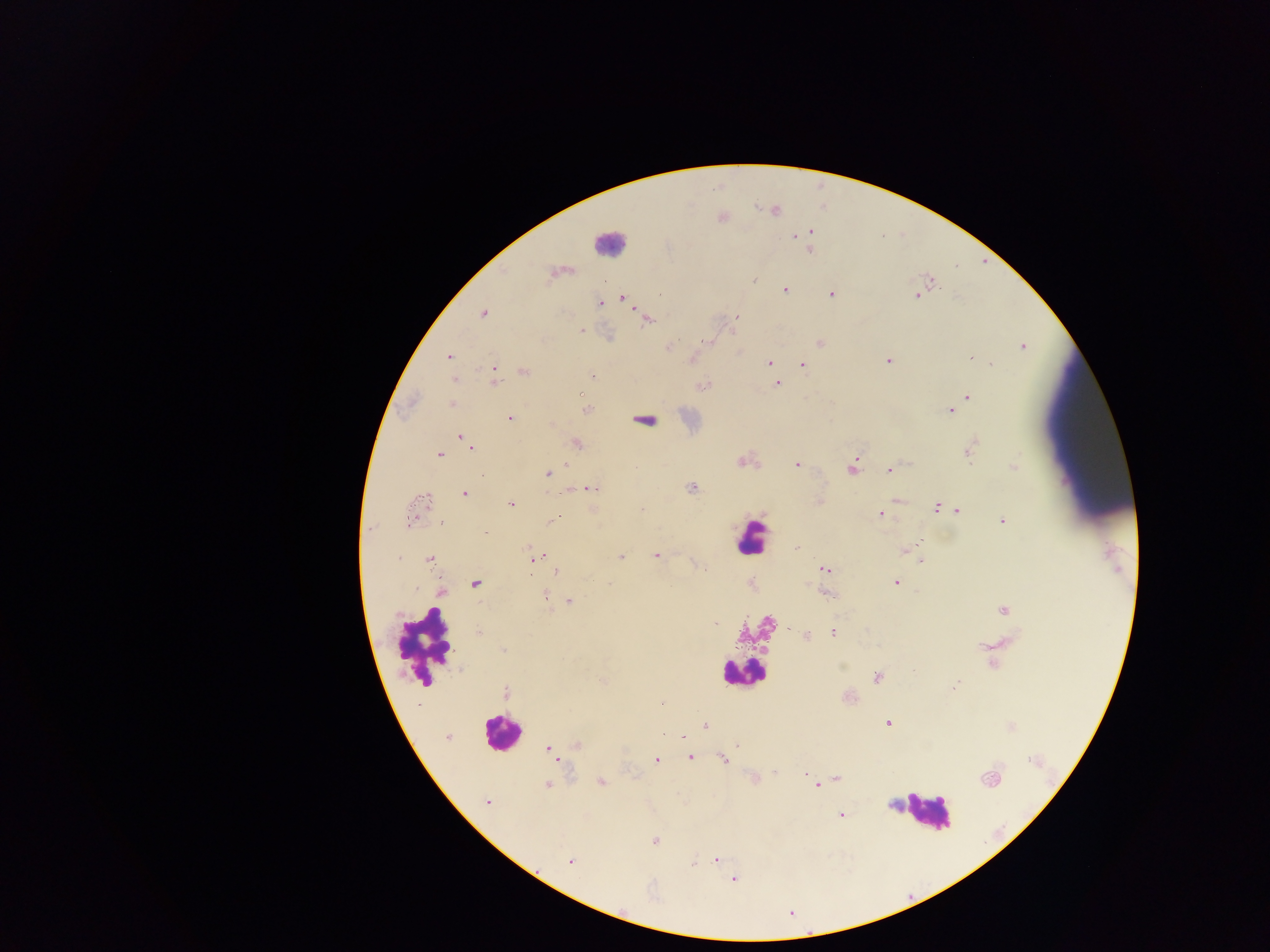

Plasmodium parasite locations = approximate centers as x y in pixels: 722 217; 811 231; 793 237; 669 248; 808 250; 563 273; 552 275; 755 280; 931 282; 786 291; 919 294; 831 295; 622 296; 914 296; 618 299; 627 300; 599 303; 483 313; 564 313; 648 321; 582 328; 819 343; 670 346; 1023 346; 971 357; 449 359; 886 359; 768 360; 803 363; 992 364; 495 373; 593 373; 589 378; 777 384; 581 395; 968 398; 451 405; 587 408; 949 410; 643 418; 512 419; 462 436; 577 443; 973 443; 469 447; 968 452; 439 454; 741 461; 798 464; 567 465; 1012 465; 851 467; 888 470; 546 472; 592 488; 691 488; 464 493; 420 503; 511 503; 642 509; 935 509; 958 511; 881 514; 553 519; 1003 520; 485 533; 915 541; 524 546; 902 551; 542 555; 656 556; 621 557; 534 559; 919 559; 431 561; 701 567; 823 569; 556 572; 896 582; 476 583; 608 583; 752 583; 807 586; 440 592; 829 594; 546 597; 569 599; 1001 609; 717 623; 833 631; 806 636; 980 646; 503 648; 990 664; 841 665; 877 678; 601 679; 956 684; 661 702; 414 704; 416 704; 887 723; 706 724; 1010 726; 684 736; 447 738; 574 745; 735 745; 547 748; 689 757; 655 759; 721 759; 774 771; 803 771; 753 777; 807 777; 989 778; 837 780; 832 781; 600 782; 548 785; 818 786; 911 794; 487 802; 891 805; 841 815; 657 841; 570 861; 694 861; 701 861; 717 861; 735 880
field of view = single
preparation = thick blood smear
leukocyte locations = approximate centers as x y in pixels: 610 242; 758 533; 420 648; 741 675; 501 730; 927 813
country = Ghana
image size = 1270×952 pixels
capture = mobile-phone photograph through a microscope